Give the position of every Plasmodium parasite.
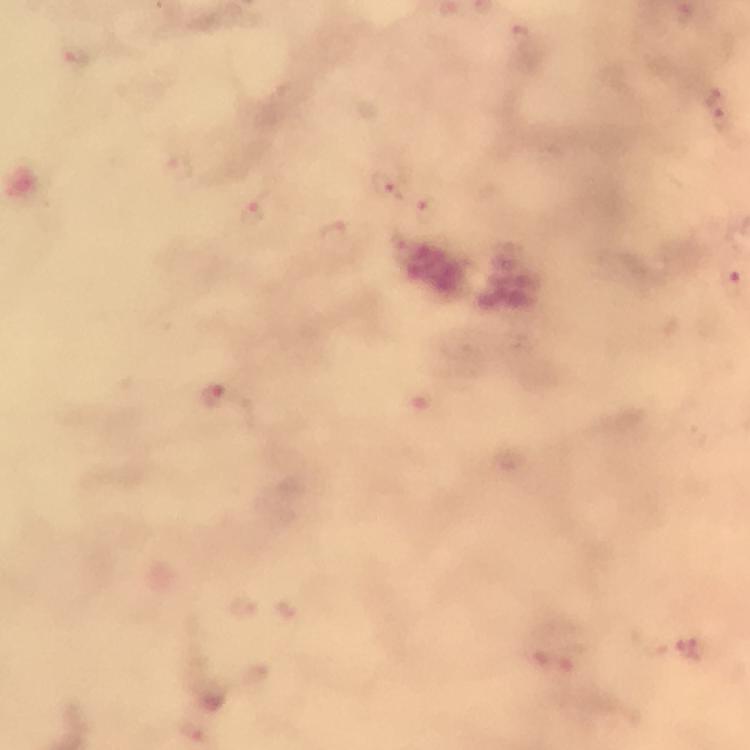
Approximate centers as {x, y} in pixels.
Plasmodium parasites: {521, 35}, {75, 55}, {712, 95}, {722, 118}, {178, 168}, {385, 188}, {427, 208}, {251, 215}, {333, 235}, {733, 285}, {211, 396}, {244, 606}.

capture = smartphone mounted on the microscope
context = from a diagnostic examination for malaria
preparation = thick smear
magnification = 100x
image size = 750×750 pixels
stain = Giemsa
immersion oil = applied
cropped from = a single field of view